Assess for malaria.
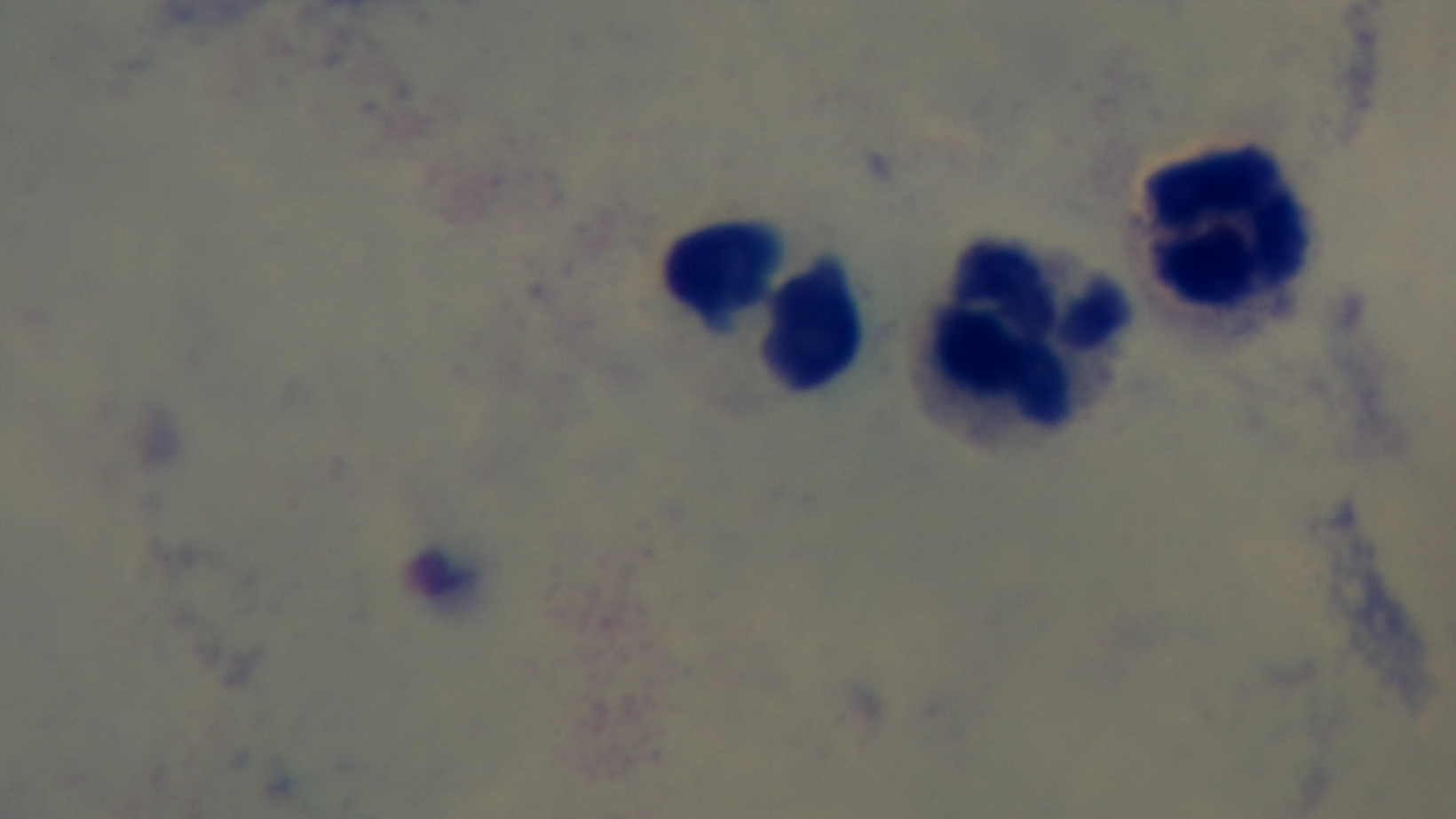

Uninfected.

Preparation: thick smear. Captured with a mounted 4K digital camera. Light microscopy. 100x oil-immersion objective. One field from the slide. Giemsa stain.